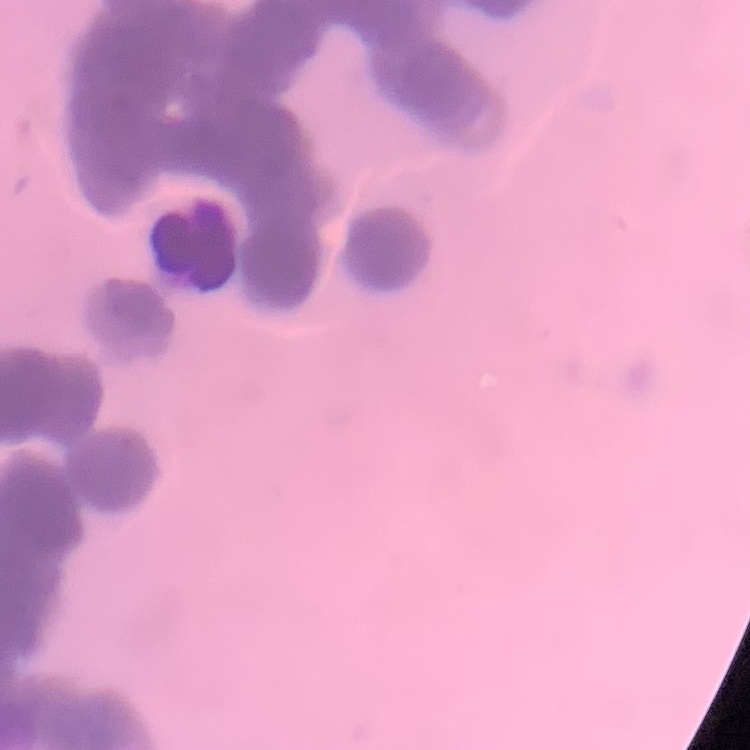 The erythrocytes exhibit rouleaux formation. Square crop of a larger photomicrograph. Stained with either Field's or Giemsa. Thin blood smear.